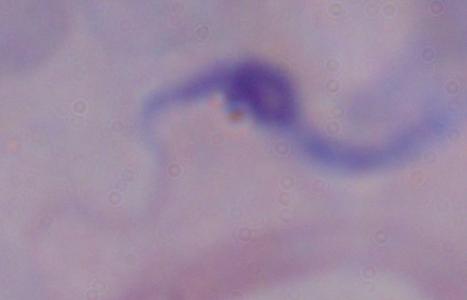

modality = photomicrograph
magnification = 1000x
identification = trypanosome